Name the cell type shown.
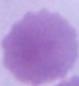

This is an erythrocyte.

modality = photomicrograph
magnification = 1000x